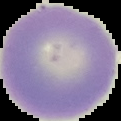
image size = 121×121 pixels
preparation = thin blood film
result = no malaria parasites seen
image type = segmented cell region with the area outside set to black